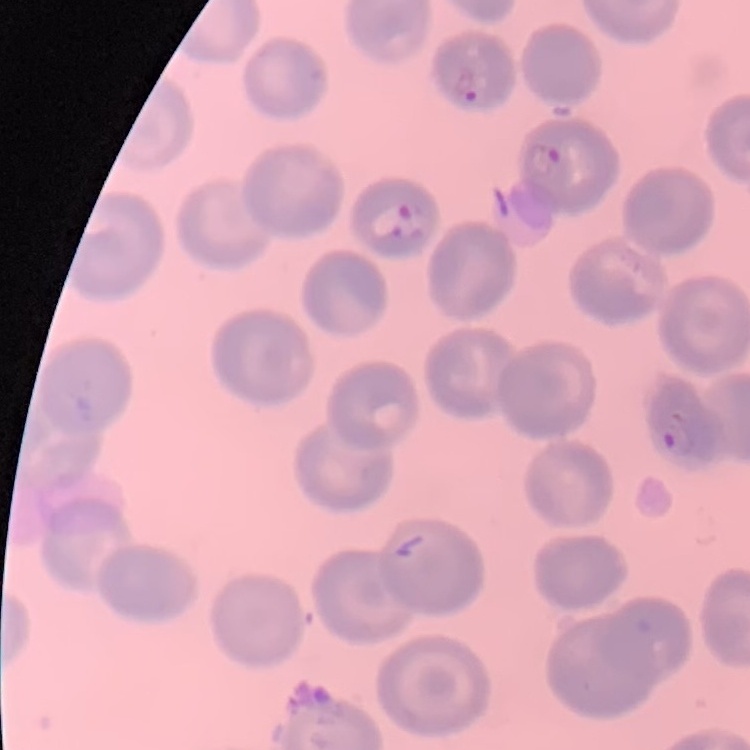
erythrocyte morphology = no rouleaux formation
image type = square crop of a larger photomicrograph
preparation = thin peripheral smear
stain = Field's or Giemsa